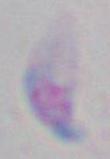

modality: micrograph
identification: Toxoplasma gondii
magnification: 1000x